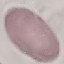

{
  "result": "negative for malaria parasites",
  "capture": "smartphone camera at the microscope eyepiece",
  "image_type": "cell patch, automatically extracted from a larger field of view and resized to 64 × 64 pixels",
  "preparation": "thin smear",
  "stain": "Giemsa"
}